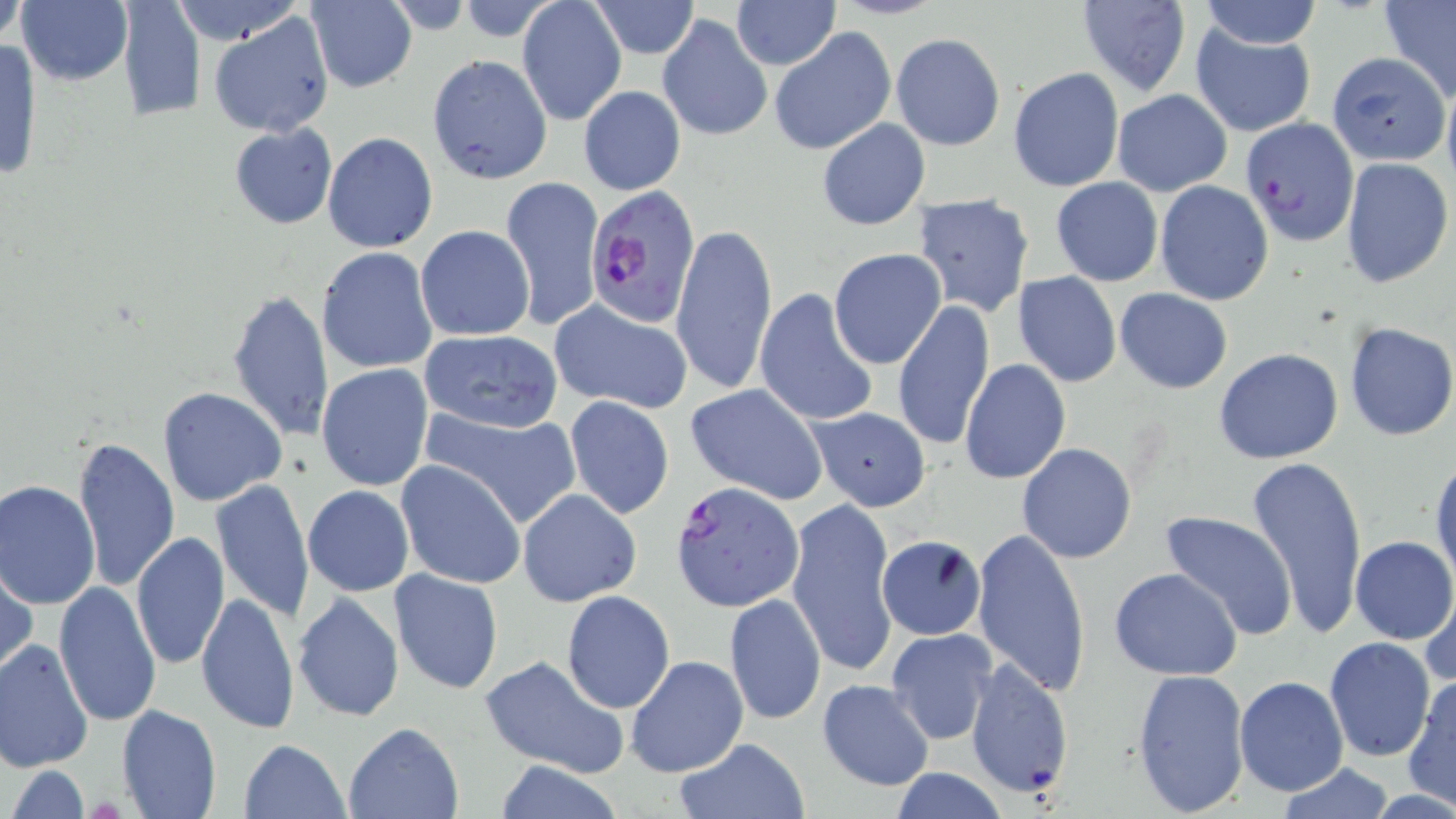

Summary:
  - Coordinate format: approximate bounding boxes as [x1, y1, x2, y2] in pixels
  - Uninfected red blood cell locations: [0, 0, 27, 51], [16, 0, 134, 86], [116, 0, 204, 122], [167, 0, 304, 45], [305, 0, 416, 94], [517, 0, 627, 124], [733, 0, 838, 70], [1196, 0, 1324, 49], [587, 1, 701, 59], [1076, 1, 1191, 97], [1380, 1, 1456, 104], [209, 10, 334, 137], [657, 14, 772, 142], [1190, 24, 1316, 136], [769, 27, 896, 157], [891, 33, 1006, 152], [0, 39, 42, 184], [1333, 45, 1450, 164], [427, 53, 553, 184], [1008, 66, 1124, 192], [579, 85, 686, 196], [1112, 88, 1232, 197], [816, 118, 930, 231], [228, 124, 339, 230], [323, 132, 438, 252], [1340, 159, 1453, 288], [501, 176, 604, 331], [1051, 176, 1163, 286], [1154, 181, 1273, 303], [914, 193, 1035, 318], [670, 222, 778, 395], [416, 225, 535, 342], [317, 247, 436, 373], [828, 248, 946, 370], [1012, 272, 1122, 388], [226, 288, 335, 443], [751, 288, 879, 428], [1115, 288, 1233, 394], [891, 298, 996, 453], [552, 302, 693, 414], [1341, 321, 1456, 442], [422, 330, 563, 434], [1213, 346, 1344, 464], [959, 359, 1070, 485], [315, 364, 433, 490], [685, 383, 829, 504], [157, 386, 287, 506], [564, 396, 675, 520], [419, 405, 579, 528], [808, 407, 931, 511], [73, 435, 179, 593], [1016, 442, 1137, 564], [1245, 454, 1369, 639], [1430, 455, 1455, 590], [396, 460, 527, 589], [1, 479, 101, 608], [210, 479, 315, 623], [303, 486, 415, 597], [518, 489, 641, 605], [786, 497, 901, 679], [1156, 512, 1299, 641], [970, 528, 1092, 697], [131, 532, 230, 671], [876, 535, 988, 640], [1351, 535, 1456, 644], [1, 558, 36, 682], [1107, 567, 1244, 680], [389, 569, 503, 694], [53, 580, 161, 727], [1421, 583, 1456, 693], [561, 590, 676, 713], [194, 591, 298, 737], [724, 592, 826, 726], [293, 593, 406, 723], [886, 628, 998, 745], [1324, 637, 1435, 762], [0, 639, 94, 772], [480, 654, 631, 780], [624, 655, 748, 779], [966, 656, 1075, 800], [1130, 667, 1251, 815], [1404, 674, 1456, 808], [1234, 676, 1348, 797], [816, 679, 936, 792], [115, 702, 222, 819], [343, 721, 465, 819], [674, 737, 810, 819], [238, 738, 351, 819], [491, 761, 626, 818], [1273, 764, 1398, 818], [6, 765, 92, 819], [888, 767, 1010, 819]
  - Plasmodium falciparum-infected red blood cell locations: [1240, 118, 1357, 246], [587, 186, 704, 326], [670, 479, 802, 610]
  - Slide-level diagnosis: Plasmodium falciparum
  - Image size: 1456×819 pixels
  - Modality: light microscopy
  - Stain: May-Grünwald-Giemsa
  - Magnification: 1000x
  - Field of view: one of a larger specimen
  - Preparation: thin blood smear